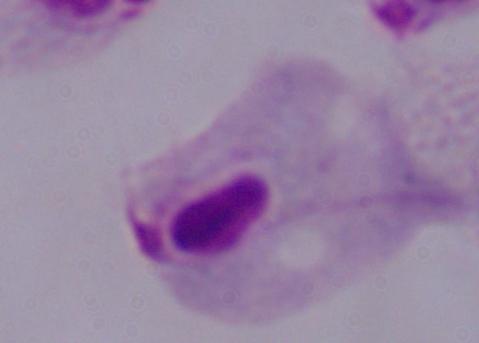

1000x magnification. A trichomonad is shown. Photomicrograph.